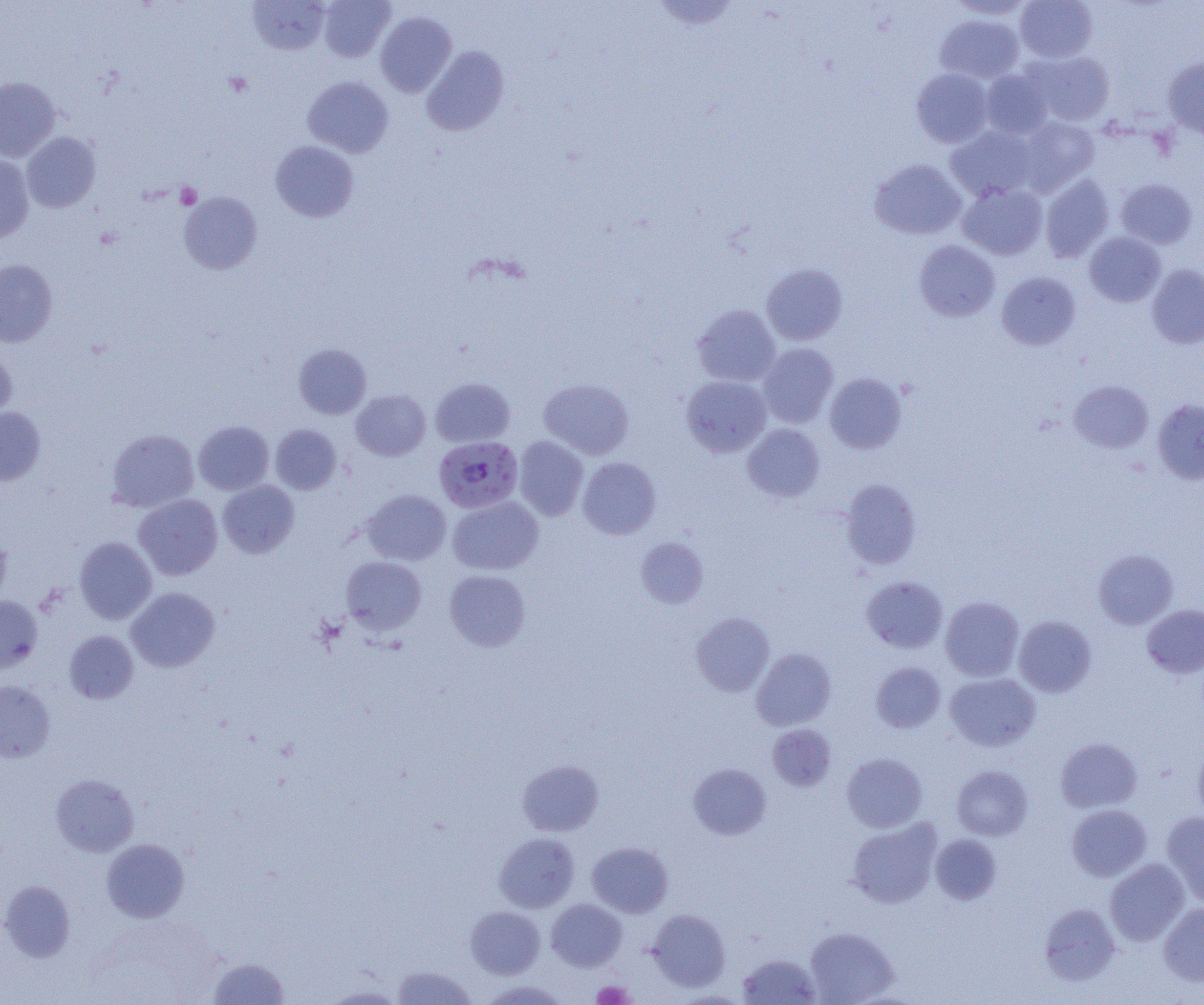

slide-level diagnosis = Plasmodium falciparum
preparation = thin blood film
Plasmodium falciparum-infected red blood cell locations = approximate bounding boxes as [x1, y1, x2, y2] in pixels: [434, 436, 523, 513]
modality = light microscopy
image size = 1204×1005 pixels
field of view = single
magnification = 1000x
platelet locations = approximate bounding boxes as [x1, y1, x2, y2] in pixels: [175, 182, 202, 209], [592, 981, 634, 1004]
uninfected red blood cell locations = approximate bounding boxes as [x1, y1, x2, y2] in pixels: [248, 0, 330, 55], [317, 0, 395, 62], [947, 0, 1035, 19], [1015, 0, 1097, 62], [651, 1, 741, 31], [375, 11, 456, 97], [935, 14, 1024, 83], [421, 45, 509, 136], [1024, 51, 1115, 127], [1163, 57, 1204, 139], [912, 68, 994, 147], [980, 69, 1053, 139], [0, 76, 60, 162], [303, 76, 394, 158], [1018, 117, 1100, 195], [946, 126, 1038, 202], [22, 132, 101, 213], [270, 140, 359, 222], [0, 154, 35, 243], [870, 159, 966, 239], [1040, 174, 1114, 263], [1116, 178, 1198, 248], [957, 183, 1048, 260], [178, 191, 262, 274], [1084, 232, 1166, 307], [914, 240, 999, 322], [0, 259, 58, 347], [762, 264, 847, 345], [1147, 264, 1204, 349], [996, 272, 1081, 350], [692, 304, 780, 387], [758, 343, 838, 428], [294, 344, 372, 419], [0, 349, 17, 424], [825, 373, 906, 453], [680, 375, 772, 457], [431, 378, 515, 447], [539, 378, 634, 459], [1069, 380, 1153, 452], [351, 390, 431, 461], [1152, 398, 1204, 484], [0, 407, 46, 486], [194, 421, 274, 495], [270, 424, 342, 494], [742, 424, 824, 502], [107, 429, 199, 512], [513, 436, 589, 521], [578, 457, 661, 540], [841, 478, 921, 569], [218, 480, 299, 558], [363, 489, 451, 565], [133, 494, 222, 580], [447, 496, 544, 574], [0, 528, 11, 606], [74, 537, 157, 624], [636, 537, 709, 608], [1093, 548, 1178, 629], [340, 556, 427, 633], [444, 569, 530, 651], [861, 576, 948, 654], [126, 588, 220, 672], [0, 596, 42, 674], [940, 596, 1024, 681], [1142, 604, 1204, 678], [691, 612, 775, 696], [1014, 616, 1097, 697], [64, 631, 139, 704], [751, 648, 836, 730], [871, 662, 945, 733], [945, 673, 1041, 751], [0, 680, 55, 763], [768, 725, 836, 791], [1055, 737, 1142, 813], [1193, 744, 1204, 823], [842, 753, 927, 832], [518, 760, 604, 836], [689, 763, 771, 839], [952, 765, 1033, 840], [50, 774, 138, 856], [1067, 804, 1152, 881], [1161, 812, 1204, 905], [848, 819, 941, 908], [494, 833, 579, 912], [931, 834, 1002, 905], [101, 838, 189, 922], [495, 838, 673, 914], [587, 842, 673, 918], [1105, 858, 1190, 945], [0, 880, 75, 962], [546, 899, 627, 971], [1039, 903, 1120, 985], [1159, 903, 1204, 986], [466, 906, 545, 978], [647, 908, 730, 991], [804, 926, 898, 1004], [738, 954, 821, 1004], [208, 957, 289, 1004], [392, 965, 477, 1004], [479, 979, 569, 1004], [322, 986, 408, 1004]